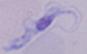 1000x magnification. A trypanosome is shown. Micrograph.